Look for parasitized red blood cells.
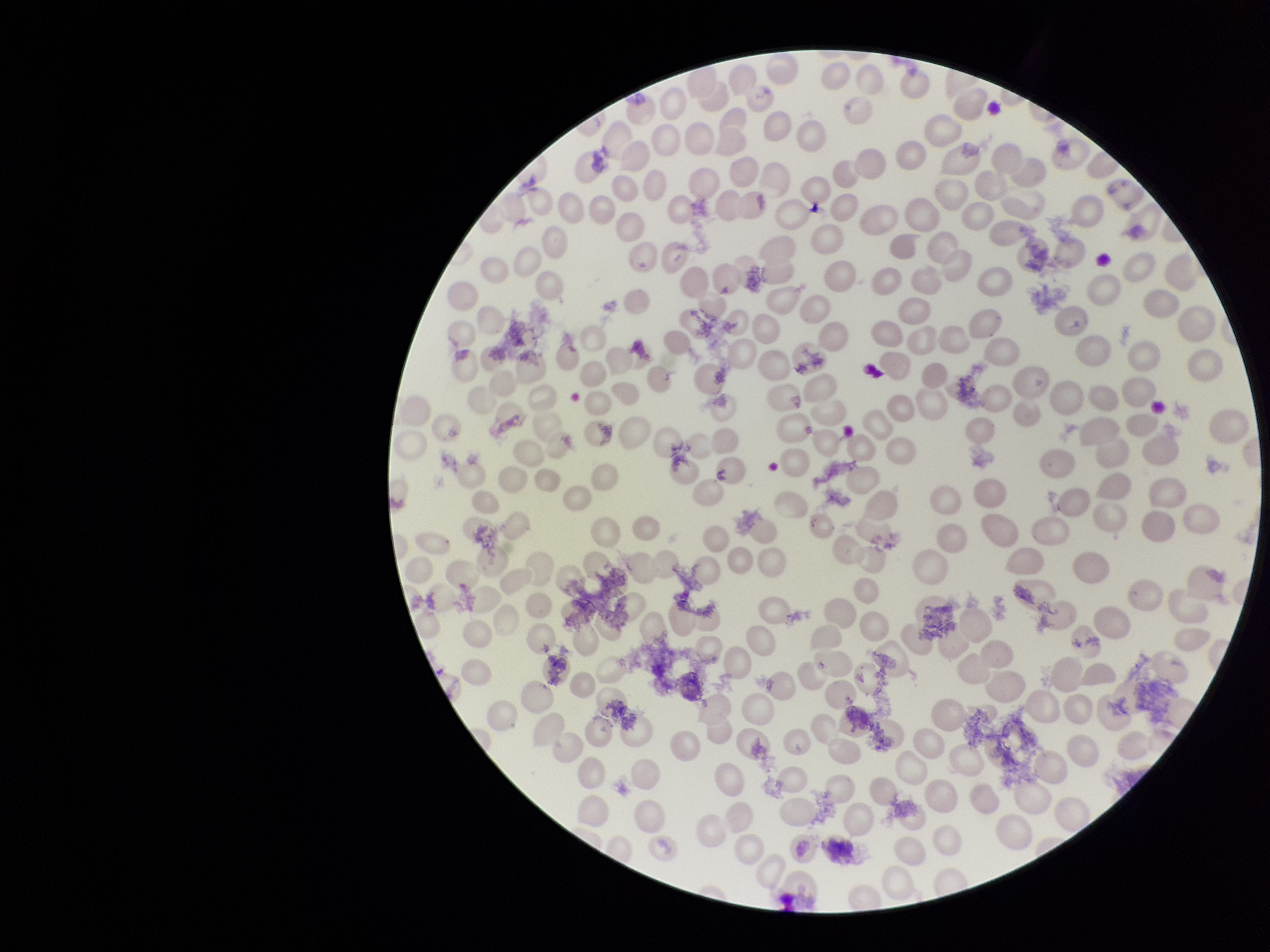
None seen.

{
  "stain": "Giemsa",
  "parasitized_red_blood_cell_count": 0,
  "capture": "smartphone photograph through the microscope eyepiece",
  "preparation": "thin",
  "red_blood_cell_count": 238,
  "patient_malaria_status": "negative",
  "field_of_view": "single",
  "image_size": "1270×952 pixels"
}